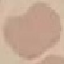
Summary:
  - Result: no malaria parasites seen
  - Capture: smartphone camera at the microscope eyepiece
  - Preparation: thin blood smear
  - Image type: cell patch, automatically extracted from a larger field of view and resized to 64 × 64 pixels
  - Stain: Giemsa